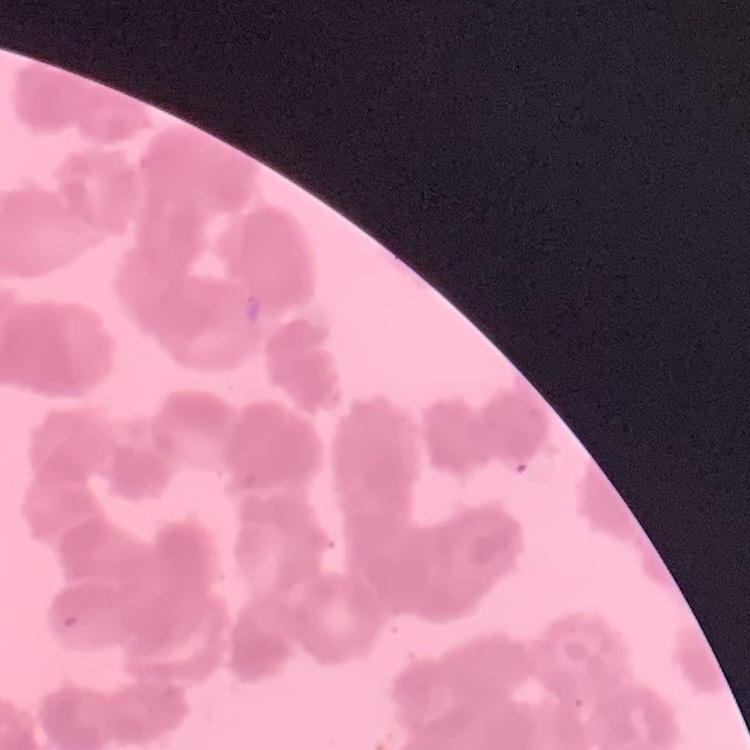

{
  "red_blood_cell_morphology": "rouleaux formation",
  "preparation": "thin blood smear",
  "image_type": "square crop of a larger photomicrograph",
  "stain": "Field's or Giemsa"
}